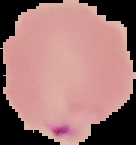 Cell region segmented out of the field of view; the surrounding area is masked to black. Image is 136×145 pixels. Malaria status: parasitized. From a thin blood film.